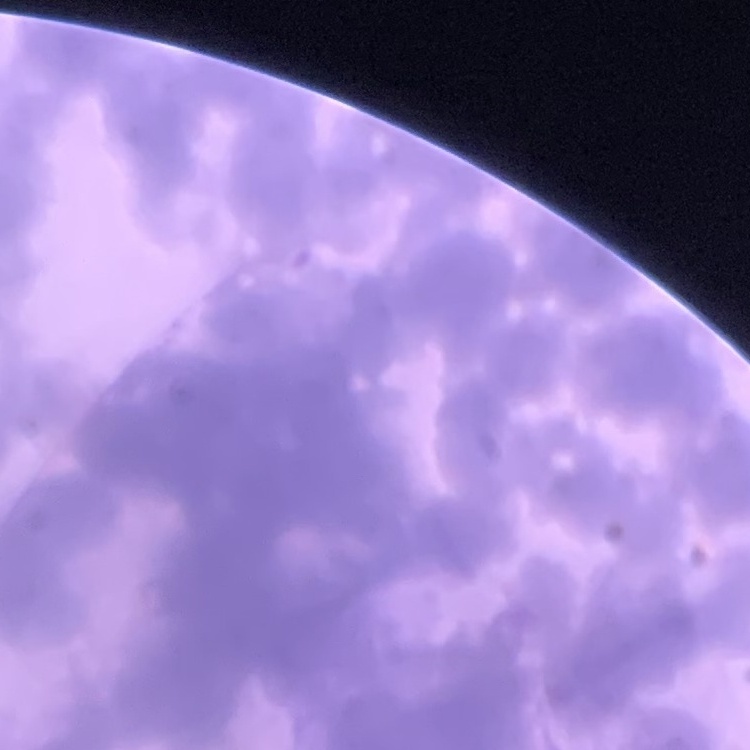 The erythrocytes exhibit rouleaux formation. Square crop of a larger photomicrograph. Stained with either Field's or Giemsa. Thin blood smear.